Locate every Plasmodium parasite.
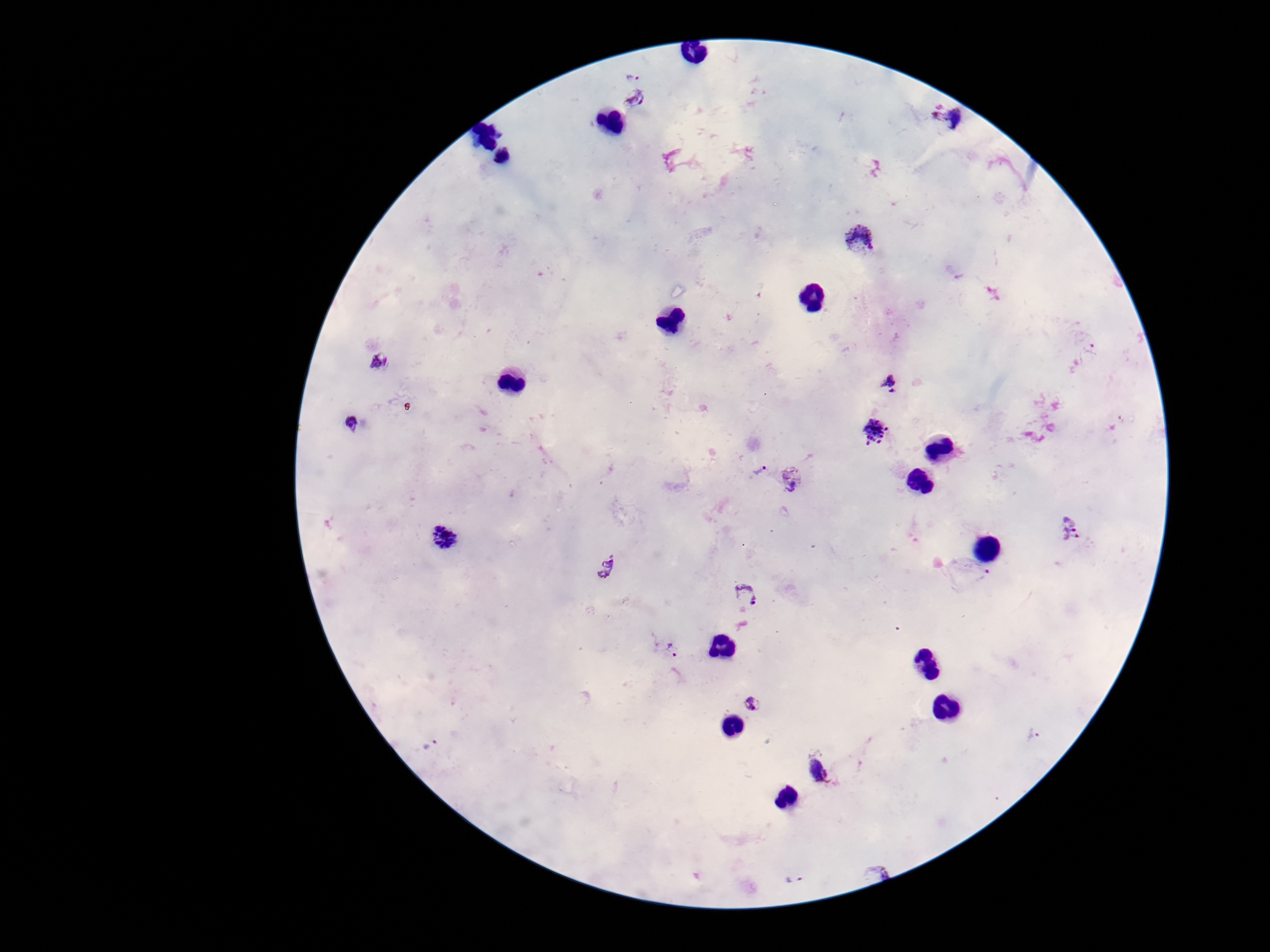
Approximate centers as {x, y} in pixels.
Plasmodium parasites: {633, 72}, {635, 103}, {948, 117}, {859, 239}, {378, 361}, {892, 382}, {353, 424}, {874, 433}, {758, 469}, {793, 482}, {1070, 527}, {443, 538}, {609, 568}, {980, 574}, {747, 596}, {673, 650}, {752, 705}, {1033, 734}, {431, 744}, {817, 769}, {877, 873}, {793, 879}.

field of view = one from this slide
preparation = thick peripheral-blood smear
stain = Giemsa
magnification = 100x
capture = smartphone camera through the microscope eyepiece
patient malaria status = positive
image size = 1270×952 pixels